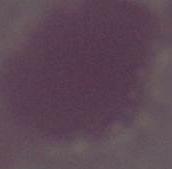

A red blood cell is shown. Captured at 1000x magnification. Micrograph.